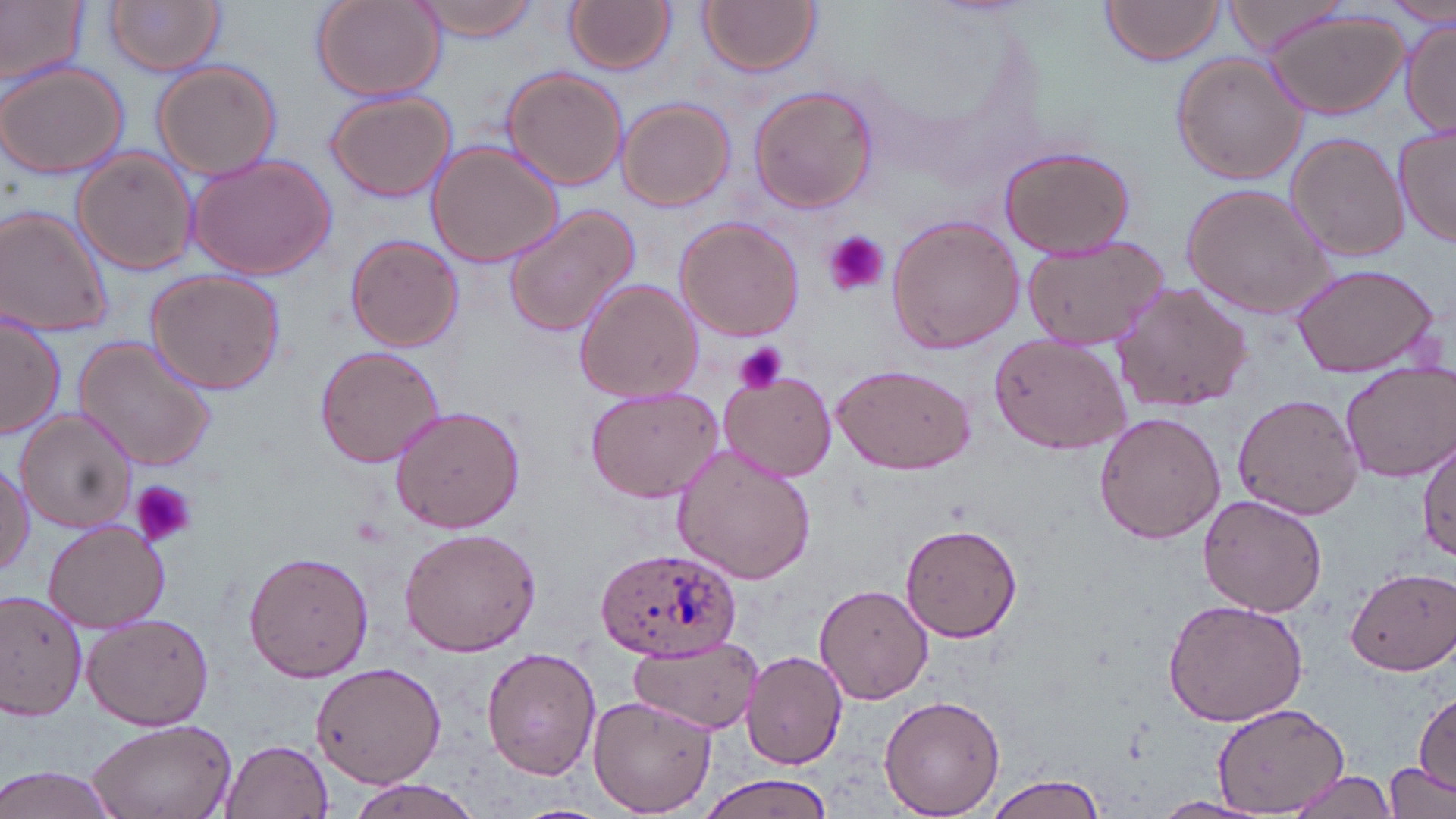
{
  "slide_level_diagnosis": "Plasmodium ovale",
  "preparation": "thin blood smear",
  "uninfected_red_blood_cell_locations": "approximate bounding boxes as (x1,y1)-(x2,y2) corner pairs in pixels: (0,0)-(87,91), (106,0)-(226,76), (412,0)-(544,42), (566,0)-(677,75), (698,0)-(821,76), (1226,0)-(1347,55), (1388,0)-(1454,26), (309,1)-(445,102), (1102,1)-(1227,66), (1264,9)-(1411,122), (1400,17)-(1456,137), (1171,53)-(1309,185), (151,61)-(282,179), (0,62)-(131,180), (501,66)-(627,191), (747,85)-(878,213), (325,90)-(457,203), (616,97)-(735,212), (1392,124)-(1455,250), (1285,132)-(1408,262), (426,140)-(563,269), (996,143)-(1137,259), (73,149)-(198,277), (188,151)-(336,281), (1178,182)-(1336,320), (502,203)-(644,340), (0,204)-(116,339), (885,215)-(1025,356), (673,216)-(806,342), (345,234)-(464,352), (1020,235)-(1171,351), (1289,262)-(1441,380), (144,268)-(286,393), (573,277)-(704,405), (1113,281)-(1254,410), (0,310)-(66,441), (990,334)-(1133,454), (72,336)-(218,472), (313,345)-(447,468), (1337,361)-(1454,482), (830,362)-(974,475), (717,369)-(838,481), (583,387)-(726,504), (1231,394)-(1364,520), (389,404)-(526,535), (16,411)-(137,534), (1093,411)-(1226,545), (1417,430)-(1454,563), (670,442)-(817,587), (0,462)-(32,579), (1198,495)-(1328,617), (44,520)-(170,632), (900,522)-(1022,644), (397,528)-(542,656), (244,549)-(374,683), (1345,566)-(1456,676), (815,582)-(933,704), (0,587)-(91,722), (1161,598)-(1308,727), (84,612)-(217,731), (633,638)-(762,730), (481,646)-(600,780), (740,649)-(848,769), (310,661)-(446,787), (1412,693)-(1455,795), (587,694)-(716,817), (879,694)-(1006,816), (1212,706)-(1349,811), (85,716)-(238,819), (221,738)-(334,819), (1386,762)-(1453,816), (0,765)-(124,819), (1287,769)-(1400,819), (983,774)-(1110,818), (696,775)-(836,818), (344,777)-(487,818), (1151,796)-(1270,818)",
  "image_size": "1456×819 pixels",
  "magnification": "1000x",
  "platelet_locations": "approximate bounding boxes as (x1,y1)-(x2,y2) corner pairs in pixels: (822,231)-(887,295), (732,342)-(788,395), (131,480)-(196,547)",
  "modality": "optical microscopy",
  "field_of_view": "one of a larger specimen",
  "stain": "May-Grünwald-Giemsa",
  "plasmodium_ovale_infected_red_blood_cell_locations": "approximate bounding boxes as (x1,y1)-(x2,y2) corner pairs in pixels: (591,544)-(738,663)"
}